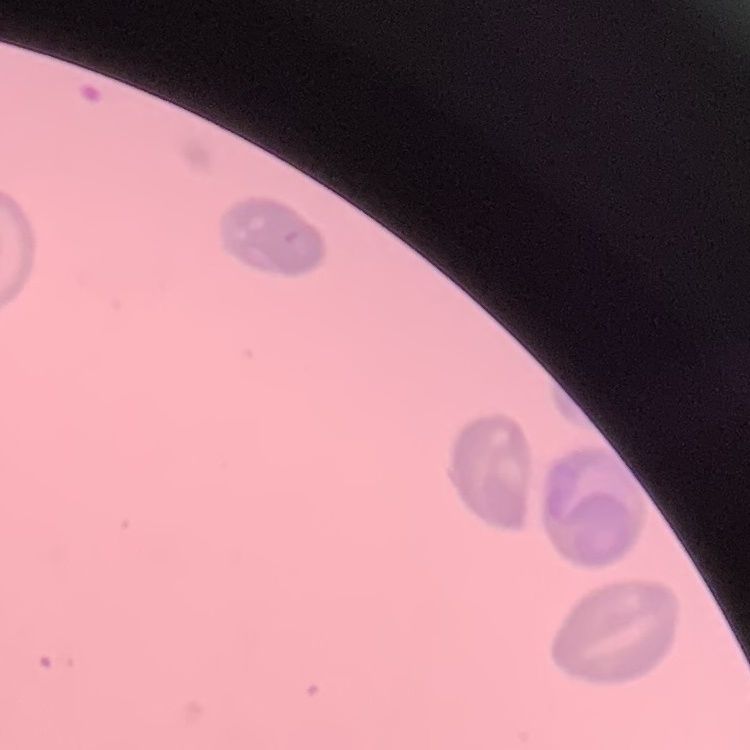

erythrocyte morphology = no rouleaux formation
preparation = thin blood film
stain = Field's or Giemsa
image type = square crop of a larger photomicrograph